Describe the morphology of the red blood cells.
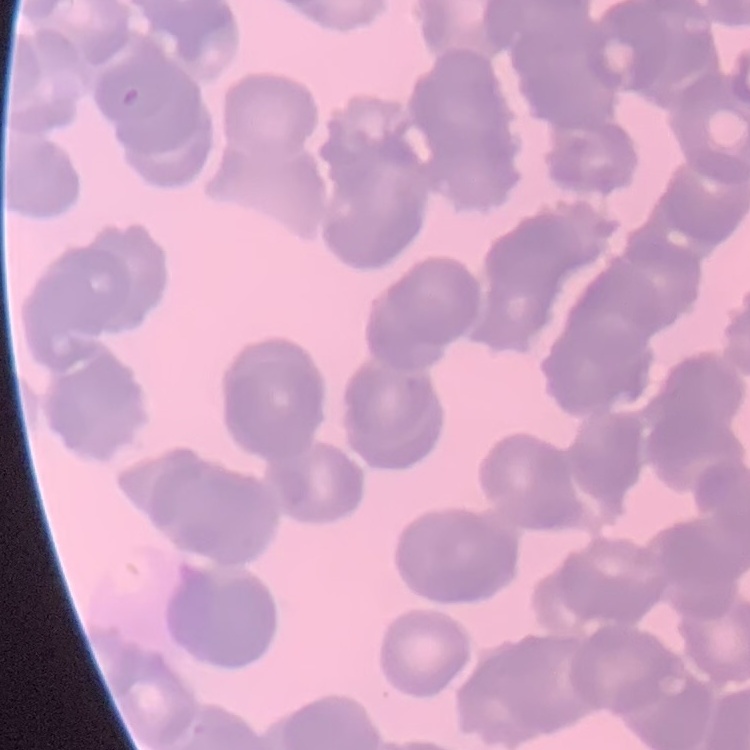

Rouleaux formation.

One tile cut from a larger photomicrograph. Thin blood film. Stained with either Field's or Giemsa.